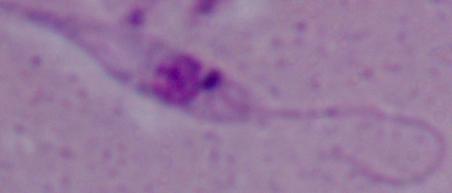
{
  "identification": "Leishmania",
  "magnification": "1000x",
  "modality": "micrograph"
}